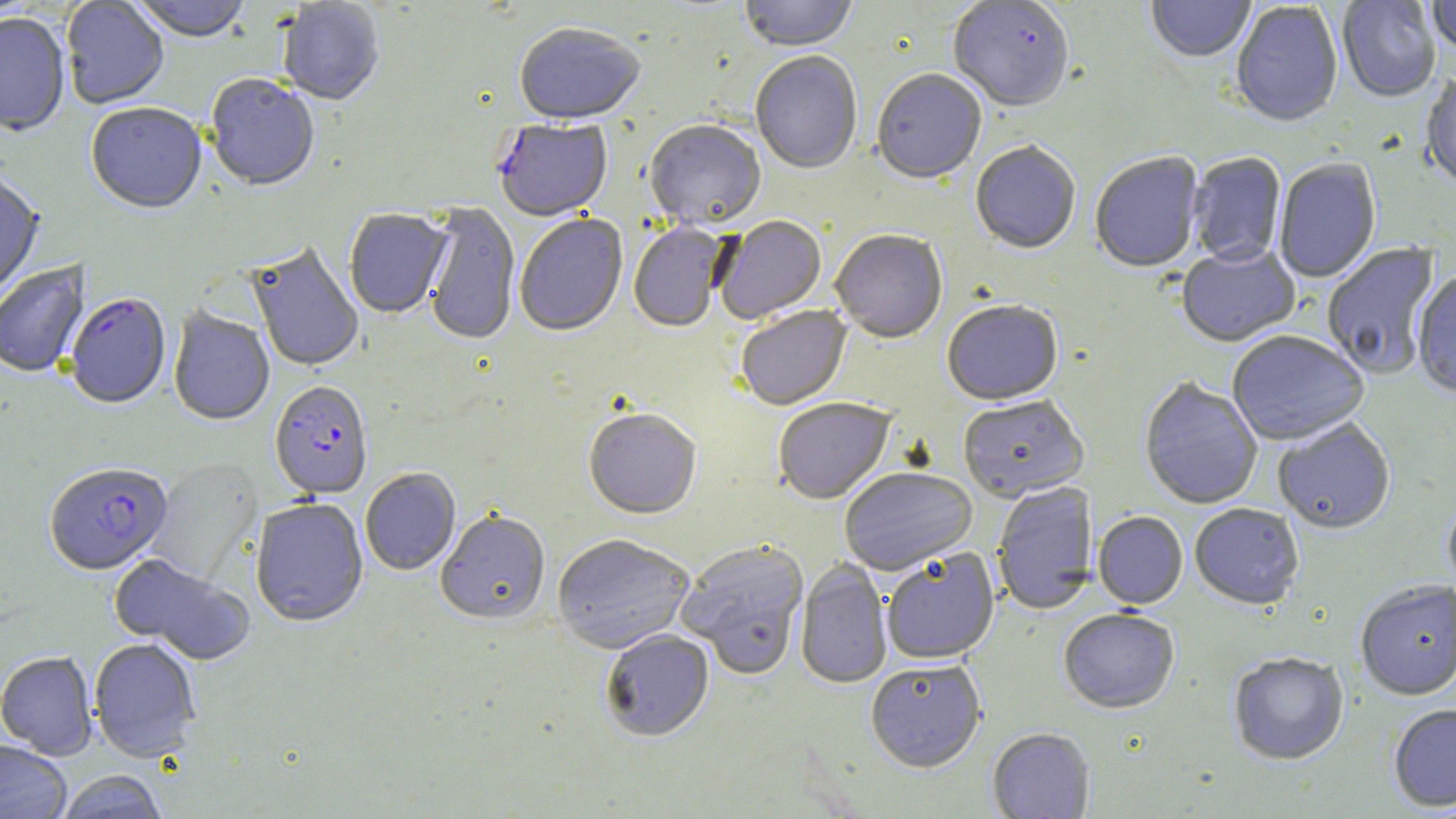

Summary:
  - Coordinate format: approximate bounding boxes as (x1, y1, x2, y2) in pixels
  - Plasmodium falciparum-infected red blood cell locations (subset): (65, 294, 171, 411), (270, 383, 373, 501), (45, 464, 173, 577)
  - Uninfected red blood cell locations (subset): (61, 0, 169, 110), (129, 0, 252, 45), (740, 0, 858, 53), (947, 0, 1075, 114), (1145, 0, 1255, 64), (1337, 0, 1440, 104), (1427, 0, 1456, 57), (277, 1, 385, 107), (1230, 2, 1343, 130), (0, 15, 70, 138), (514, 26, 645, 128), (750, 53, 863, 176), (871, 71, 987, 187), (204, 76, 320, 193), (1421, 76, 1456, 193), (86, 105, 207, 216), (644, 122, 766, 233), (970, 143, 1081, 256), (1090, 153, 1205, 274), (1188, 153, 1286, 267), (1274, 159, 1381, 283), (0, 172, 44, 302), (422, 203, 519, 347), (345, 210, 452, 320), (514, 215, 629, 339), (715, 216, 827, 325), (629, 223, 731, 334), (830, 232, 948, 345), (1322, 242, 1440, 380), (247, 243, 363, 373), (1177, 246, 1300, 349), (0, 261, 90, 380), (1412, 271, 1456, 400), (942, 302, 1063, 407), (736, 307, 852, 412), (168, 308, 274, 427), (1227, 332, 1369, 447), (1139, 379, 1262, 511), (958, 397, 1089, 504), (773, 399, 895, 506), (584, 410, 701, 522), (1273, 420, 1396, 536), (147, 458, 263, 587), (360, 469, 461, 576), (840, 469, 978, 577), (992, 482, 1098, 616), (1443, 497, 1456, 602), (250, 499, 368, 629), (1190, 505, 1304, 612), (435, 511, 550, 628), (1093, 513, 1187, 611), (552, 536, 694, 656), (677, 541, 810, 680), (882, 550, 1000, 666), (109, 553, 255, 666), (795, 558, 892, 690), (1355, 582, 1456, 702), (1059, 611, 1179, 715), (601, 631, 715, 744), (89, 638, 201, 763), (0, 652, 98, 761), (1228, 654, 1349, 767), (866, 663, 985, 775), (1388, 706, 1456, 812), (987, 729, 1095, 819), (0, 741, 72, 819), (54, 771, 169, 819)
  - Slide-level diagnosis: Plasmodium falciparum
  - Stain: May-Grünwald-Giemsa
  - Modality: optical microscopy
  - Image size: 1456×819 pixels
  - Field of view: single
  - Magnification: 1000x
  - Preparation: thin blood smear